Give the extent of all uninfected red blood cells.
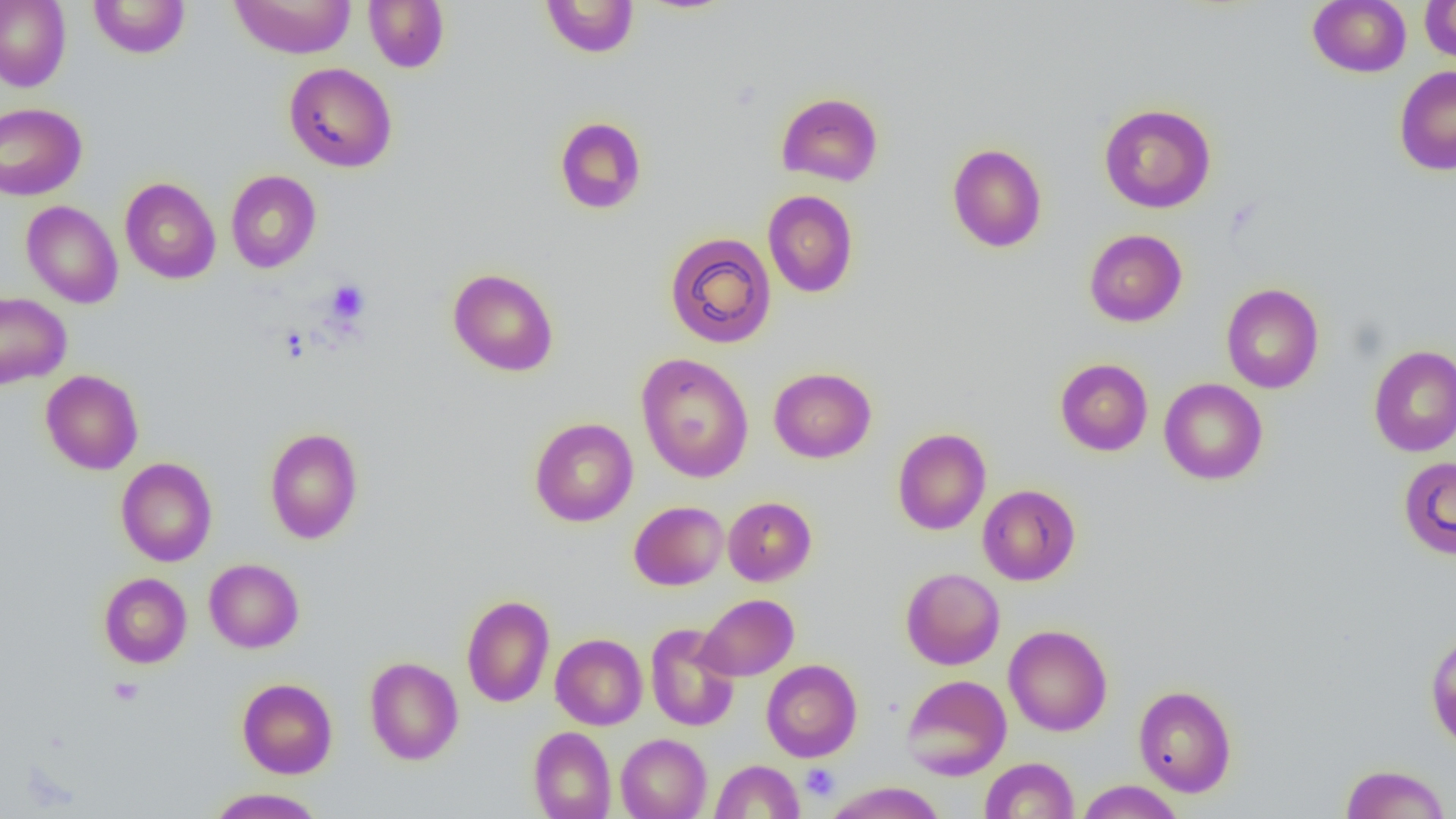

Approximate bounding boxes as named x1/y1/x2/y2 corners in pixels.
Uninfected red blood cells: (x1=0, y1=0, x2=71, y2=91), (x1=88, y1=0, x2=190, y2=58), (x1=229, y1=0, x2=356, y2=59), (x1=540, y1=0, x2=639, y2=58), (x1=1308, y1=0, x2=1411, y2=77), (x1=1419, y1=0, x2=1456, y2=63), (x1=364, y1=1, x2=450, y2=73), (x1=284, y1=62, x2=397, y2=172), (x1=1394, y1=66, x2=1456, y2=175), (x1=776, y1=92, x2=883, y2=186), (x1=0, y1=102, x2=87, y2=201), (x1=1099, y1=103, x2=1216, y2=213), (x1=554, y1=116, x2=647, y2=215), (x1=947, y1=143, x2=1047, y2=253), (x1=225, y1=170, x2=321, y2=273), (x1=120, y1=177, x2=221, y2=283), (x1=763, y1=190, x2=858, y2=297), (x1=21, y1=201, x2=123, y2=308), (x1=1084, y1=229, x2=1187, y2=326), (x1=664, y1=232, x2=777, y2=348), (x1=447, y1=268, x2=559, y2=377), (x1=1221, y1=284, x2=1324, y2=393), (x1=0, y1=291, x2=71, y2=390), (x1=1368, y1=344, x2=1456, y2=457), (x1=636, y1=353, x2=755, y2=483), (x1=1055, y1=358, x2=1153, y2=456), (x1=769, y1=367, x2=877, y2=463), (x1=40, y1=369, x2=143, y2=475), (x1=1159, y1=378, x2=1268, y2=485), (x1=529, y1=417, x2=638, y2=526), (x1=264, y1=428, x2=363, y2=544), (x1=892, y1=428, x2=991, y2=535), (x1=1398, y1=456, x2=1456, y2=560), (x1=116, y1=457, x2=217, y2=567), (x1=977, y1=484, x2=1080, y2=585), (x1=723, y1=496, x2=816, y2=586), (x1=629, y1=501, x2=728, y2=590), (x1=204, y1=558, x2=304, y2=653), (x1=901, y1=567, x2=1005, y2=670), (x1=99, y1=573, x2=191, y2=668), (x1=461, y1=594, x2=555, y2=708), (x1=697, y1=594, x2=799, y2=681), (x1=645, y1=622, x2=740, y2=731), (x1=1003, y1=624, x2=1113, y2=736), (x1=1425, y1=629, x2=1456, y2=752), (x1=551, y1=633, x2=647, y2=730), (x1=364, y1=657, x2=463, y2=765), (x1=761, y1=659, x2=862, y2=762), (x1=900, y1=674, x2=1011, y2=779), (x1=237, y1=677, x2=337, y2=779), (x1=1133, y1=684, x2=1237, y2=797), (x1=528, y1=726, x2=617, y2=819), (x1=616, y1=733, x2=712, y2=819), (x1=980, y1=757, x2=1079, y2=818), (x1=710, y1=760, x2=804, y2=818), (x1=1340, y1=764, x2=1451, y2=819), (x1=1075, y1=780, x2=1184, y2=818), (x1=824, y1=782, x2=947, y2=819), (x1=205, y1=787, x2=326, y2=819).

slide-level diagnosis = no evidence of blood parasites
preparation = thin blood smear
magnification = 1000x
modality = optical microscopy
field of view = single
platelet locations = approximate bounding boxes as named x1/y1/x2/y2 corners in pixels: (x1=326, y1=280, x2=370, y2=324), (x1=108, y1=677, x2=144, y2=706), (x1=801, y1=763, x2=839, y2=801)
image size = 1456×819 pixels